Name the parasite shown.
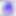

Toxoplasma gondii.

Captured at 400x magnification. Photomicrograph.